State which parasite is depicted.
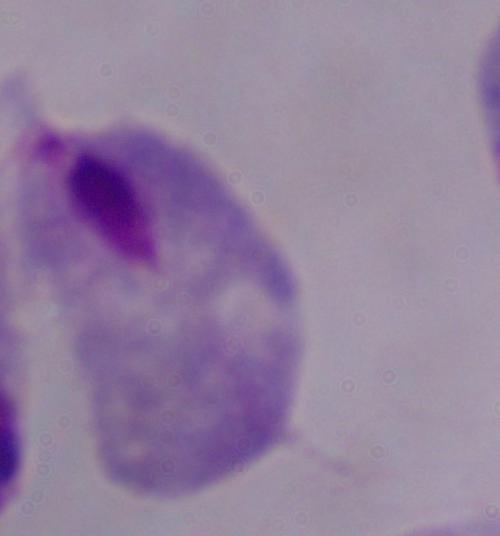
A trichomonad.

Captured at 1000x magnification. Photomicrograph.